Identify the cell.
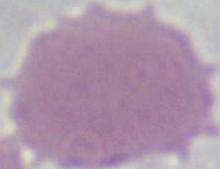

An erythrocyte.

1000x magnification. Photomicrograph.